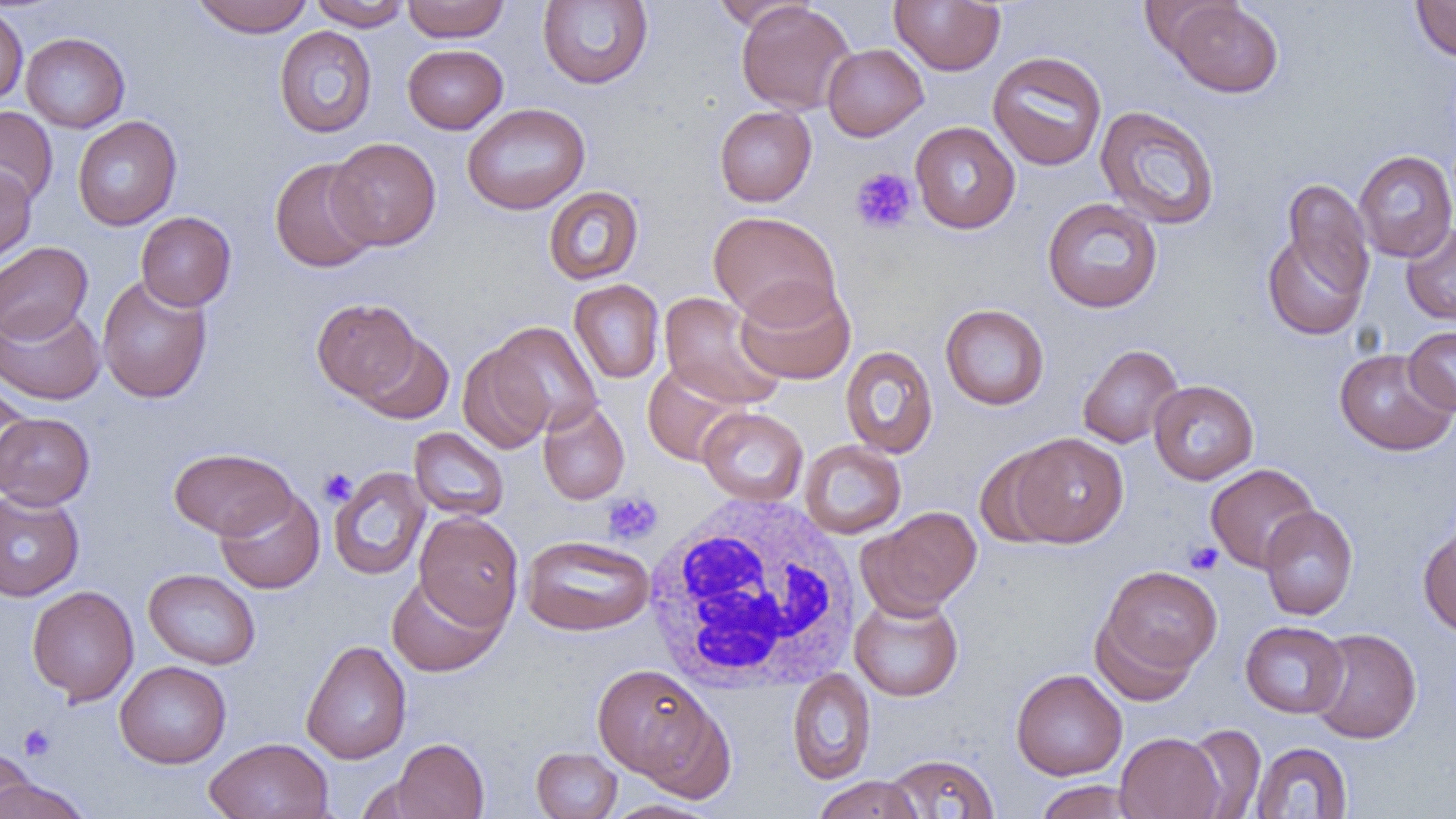 Approximate bounding boxes as (x1, y1, x2, y2) in pixels. Platelet locations: (850, 167, 918, 235), (318, 467, 358, 507), (602, 492, 663, 546), (1185, 541, 1223, 575), (18, 723, 56, 761). White blood cell locations: (641, 493, 864, 695). Uninfected red blood cell locations: (191, 0, 314, 37), (401, 0, 510, 42), (890, 0, 1006, 75), (311, 1, 410, 31), (537, 1, 654, 89), (715, 1, 813, 30), (736, 1, 856, 115), (1164, 1, 1284, 98), (1410, 1, 1456, 61), (0, 6, 28, 106), (274, 25, 378, 138), (21, 32, 129, 133), (822, 43, 928, 141), (402, 44, 507, 134), (988, 51, 1107, 171), (462, 103, 590, 215), (0, 106, 58, 207), (714, 106, 817, 206), (1095, 106, 1221, 230), (72, 116, 182, 230), (909, 121, 1021, 234), (327, 137, 441, 250), (1354, 150, 1456, 262), (269, 157, 379, 273), (0, 165, 37, 267), (1282, 179, 1374, 297), (543, 186, 644, 285), (1042, 197, 1163, 313), (135, 211, 236, 311), (708, 211, 841, 325), (1401, 223, 1456, 325), (1261, 230, 1369, 341), (0, 241, 93, 343), (96, 274, 213, 404), (735, 278, 856, 385), (569, 279, 665, 383), (659, 292, 785, 410), (312, 298, 422, 403), (0, 303, 105, 405), (940, 304, 1049, 410), (489, 321, 602, 436), (1403, 326, 1456, 414), (355, 332, 454, 423), (458, 343, 555, 454), (1077, 344, 1184, 449), (840, 346, 938, 458), (1333, 348, 1456, 456), (642, 362, 748, 466), (1148, 380, 1259, 485), (0, 382, 34, 492), (537, 399, 630, 505), (698, 407, 808, 506), (0, 412, 95, 509), (408, 428, 509, 522), (1009, 432, 1129, 547), (799, 439, 907, 538), (974, 446, 1069, 548), (169, 447, 298, 539), (1206, 463, 1319, 573), (329, 466, 430, 581), (215, 487, 325, 594), (0, 490, 84, 601), (1260, 505, 1358, 621), (860, 506, 982, 616), (414, 511, 524, 629), (1418, 525, 1456, 638), (521, 534, 655, 636), (1096, 565, 1223, 685), (143, 568, 261, 670), (385, 573, 506, 677), (26, 585, 139, 705), (849, 593, 964, 702), (1240, 621, 1349, 718), (1307, 627, 1422, 744), (300, 640, 412, 764), (115, 661, 231, 768), (592, 664, 718, 783), (1011, 668, 1127, 780), (787, 669, 876, 784), (636, 704, 737, 804), (1181, 723, 1266, 818), (1116, 732, 1225, 819), (204, 737, 334, 819), (391, 738, 489, 819), (1251, 742, 1352, 818), (531, 746, 622, 818), (0, 748, 37, 819), (884, 753, 1000, 818), (812, 776, 924, 819), (1, 777, 91, 819), (1034, 780, 1138, 818), (603, 799, 719, 819). Slide-level diagnosis: negative for blood parasites. Light microscopy. 1000x magnification. Thin blood smear. Single field of view. Image is 1456×819 pixels.